Report the malaria status of this cell.
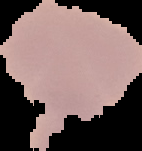
It is uninfected.

image size = 142×151 pixels
image type = cell region segmented out of the field of view; surrounding area masked to black
preparation = thin blood smear